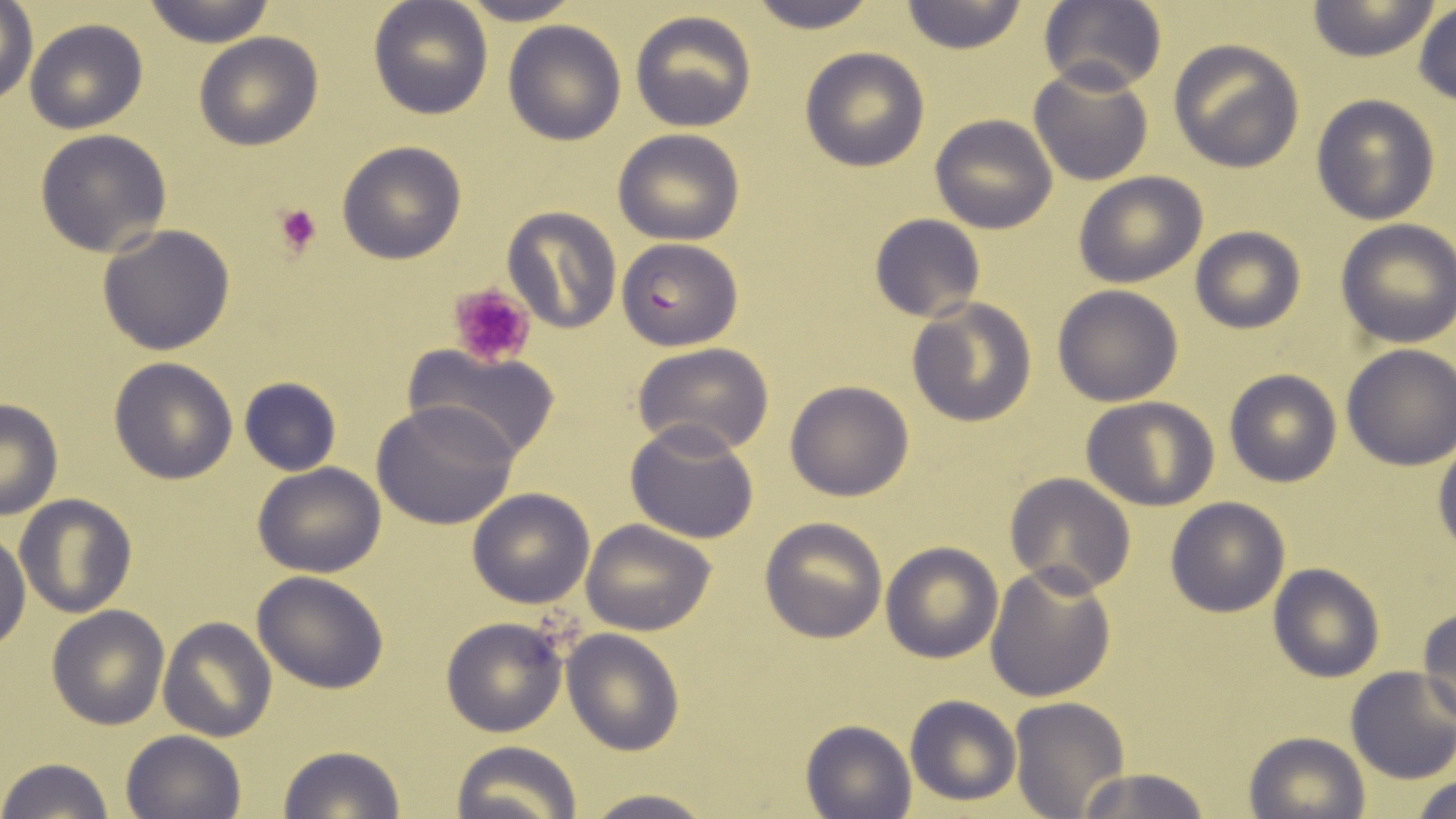

{
  "slide_level_diagnosis": "Plasmodium falciparum",
  "uninfected_red_blood_cell_locations": "approximate bounding boxes as (x1,y1)-(x2,y2) corner pairs in pixels: (141,0)-(277,46), (368,0)-(492,119), (452,0)-(585,25), (745,0)-(880,33), (899,1)-(1029,53), (1039,1)-(1166,96), (1306,1)-(1442,62), (0,3)-(38,105), (1412,4)-(1456,106), (630,10)-(756,132), (24,18)-(147,134), (503,21)-(625,145), (194,32)-(324,151), (1167,38)-(1306,173), (799,47)-(929,171), (1028,63)-(1154,187), (1310,94)-(1441,225), (930,114)-(1057,234), (612,128)-(744,245), (34,129)-(172,256), (337,141)-(467,264), (1073,172)-(1208,287), (501,206)-(620,334), (869,214)-(986,323), (1335,218)-(1456,348), (97,224)-(236,355), (1189,227)-(1306,333), (1052,285)-(1185,406), (906,298)-(1038,426), (404,345)-(561,462), (633,345)-(773,458), (1341,346)-(1456,469), (109,356)-(239,483), (1224,369)-(1341,487), (238,376)-(341,476), (784,381)-(914,501), (1082,396)-(1220,511), (0,400)-(63,519), (371,403)-(519,530), (627,420)-(758,543), (1433,440)-(1456,559), (253,462)-(386,579), (1005,473)-(1135,595), (468,488)-(596,608), (15,494)-(136,617), (1165,497)-(1290,617), (759,517)-(888,643), (581,520)-(718,636), (0,521)-(30,653), (880,541)-(1003,663), (984,562)-(1117,704), (1267,563)-(1385,682), (250,570)-(391,695), (46,604)-(170,730), (1417,607)-(1456,725), (440,616)-(567,737), (158,617)-(277,742), (563,628)-(685,756), (1344,667)-(1456,783), (905,694)-(1021,806), (1008,696)-(1129,818), (802,718)-(917,819), (121,730)-(245,819), (1243,730)-(1370,819), (448,740)-(581,819), (278,746)-(405,819), (0,758)-(118,819), (1074,766)-(1212,819), (1409,772)-(1455,819), (577,789)-(720,819)",
  "magnification": "1000x",
  "field_of_view": "single",
  "stain": "May-Grünwald-Giemsa",
  "image_size": "1456×819 pixels",
  "plasmodium_falciparum_infected_red_blood_cell_locations": "approximate bounding boxes as (x1,y1)-(x2,y2) corner pairs in pixels: (617,237)-(743,350)",
  "modality": "optical microscopy",
  "platelet_locations": "approximate bounding boxes as (x1,y1)-(x2,y2) corner pairs in pixels: (272,203)-(322,257), (447,282)-(537,368)",
  "preparation": "thin blood smear"
}